Classify this cell by malaria status.
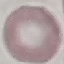

It is uninfected.

Automatically extracted cell patch, resized to 64 × 64 pixels. Thin smear of blood. Giemsa-stained preparation. Photographed with a smartphone camera at the microscope eyepiece.